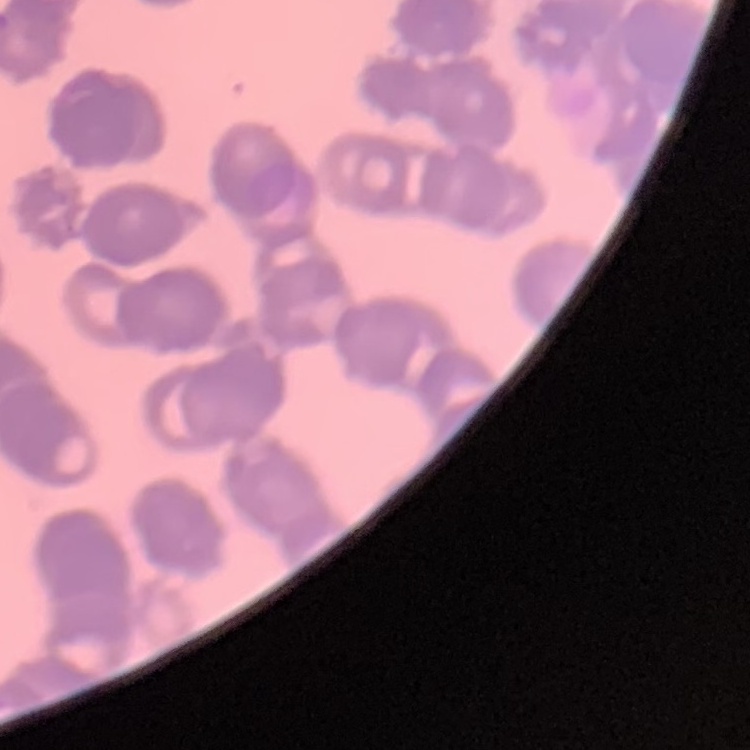

Summary:
  - Red blood cell morphology: rouleaux formation
  - Image type: square crop of a larger photomicrograph
  - Preparation: thin blood smear
  - Stain: Field's or Giemsa